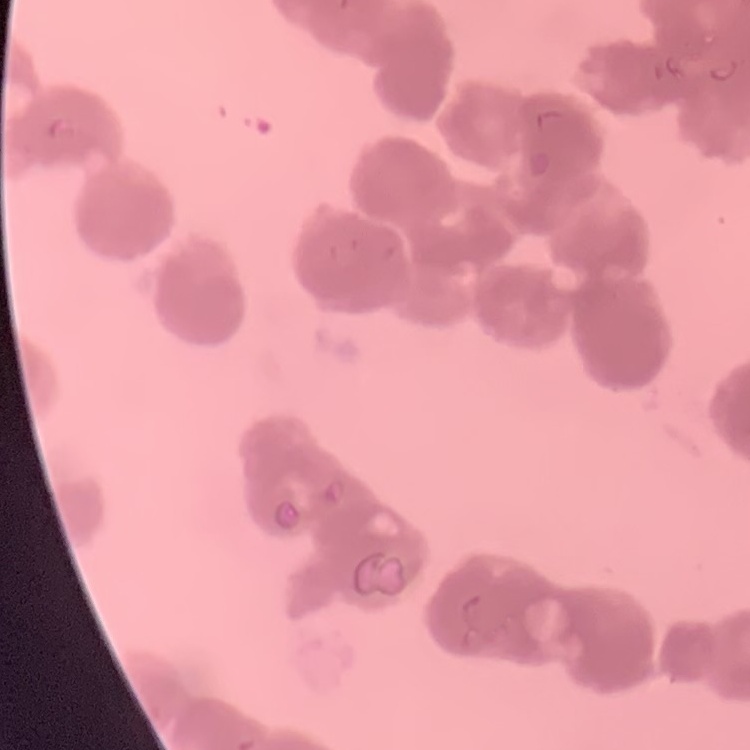
Summary:
  - Red blood cell morphology: rouleaux formation
  - Preparation: thin peripheral smear
  - Stain: Field's or Giemsa
  - Image type: square crop of a larger photomicrograph